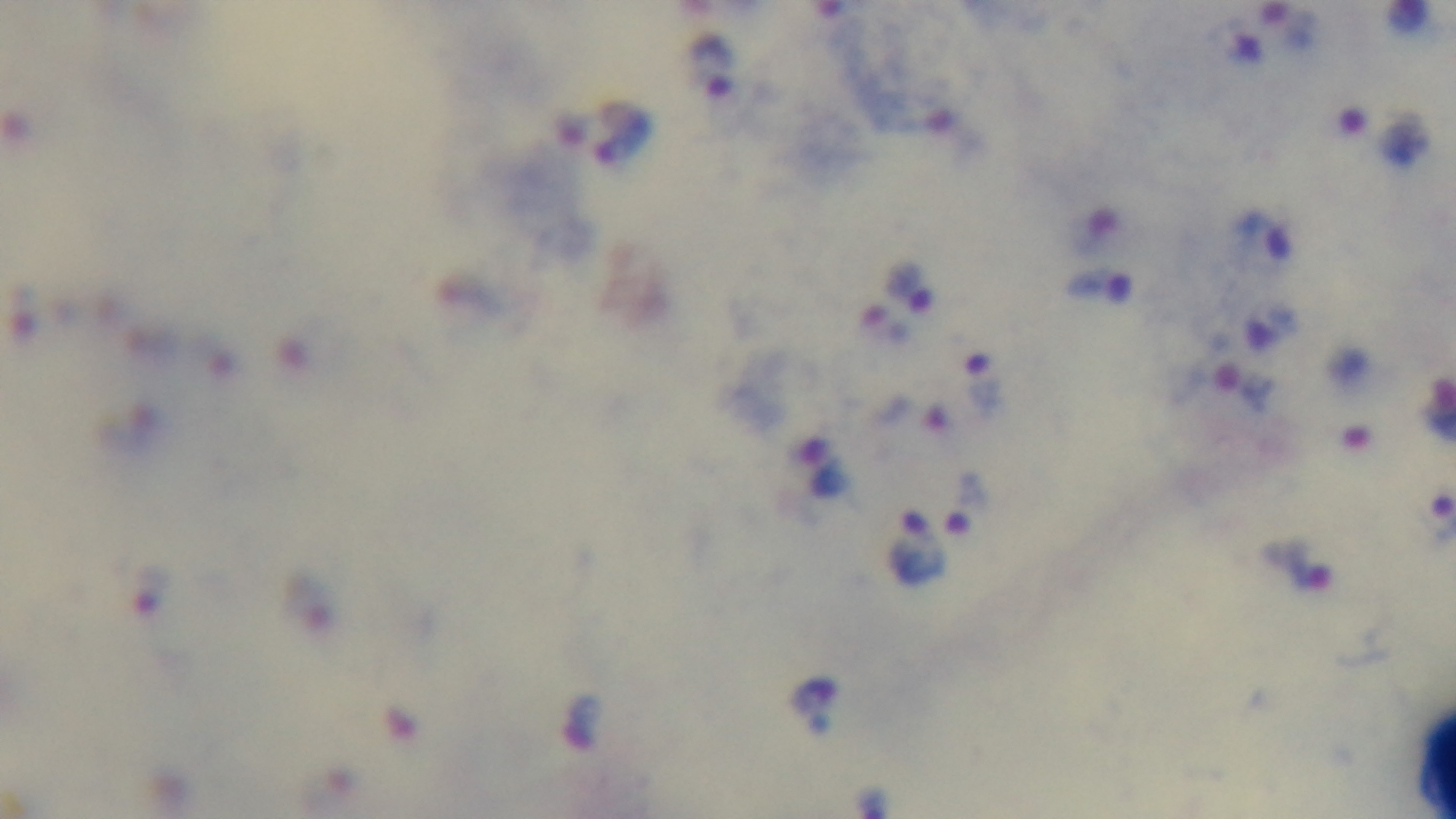
stain = Giemsa
field of view = single
preparation = thick
modality = light microscopy
capture = mounted 4K digital camera
malaria status = positive
objective = 100x oil immersion